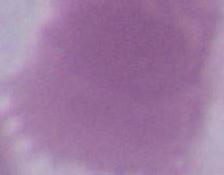

Micrograph. A red blood cell is shown. 1000x magnification.